State which parasite is depicted.
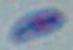

This is Toxoplasma gondii.

{
  "modality": "photomicrograph",
  "magnification": "1000x"
}